Assess this cell for malaria.
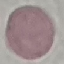
Uninfected.

image type = cell patch, automatically extracted from a larger field of view and resized to 64 × 64 pixels
preparation = thin smear
capture = smartphone through the microscope eyepiece
stain = Giemsa